Comment on the morphology of the red blood cells.
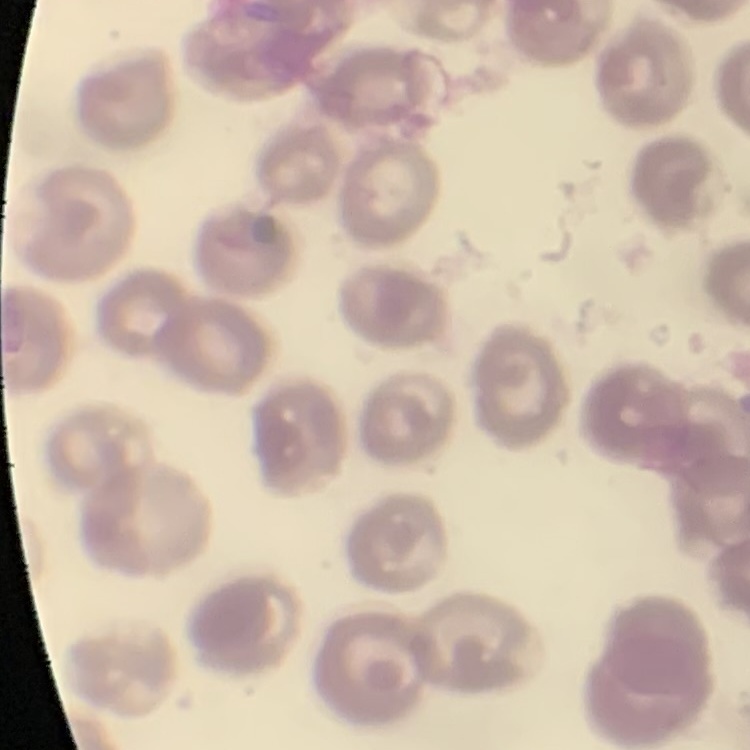

No rouleaux formation.

preparation = thin blood film
image type = one tile cut from a larger photomicrograph
stain = Field's or Giemsa